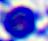 Photomicrograph. A leukocyte is shown. Captured at 400x magnification.